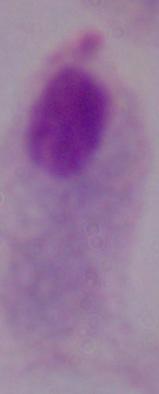 A trichomonad is seen. Captured at 1000x magnification. Micrograph.